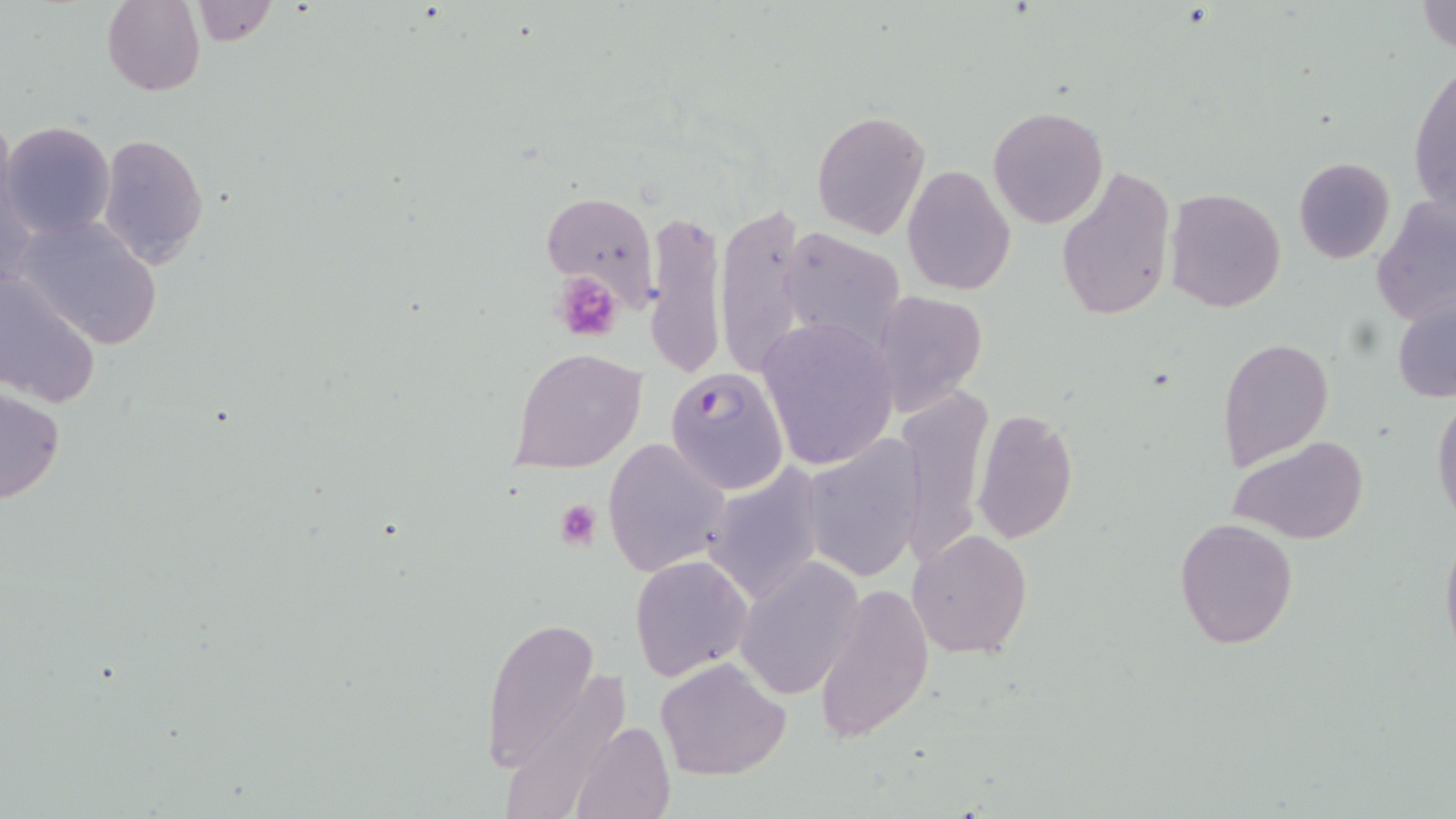

Summary:
  - Coordinate format: approximate bounding boxes as named x1/y1/x2/y2 corners in pixels
  - Platelet locations: (x1=551, y1=271, x2=627, y2=344), (x1=553, y1=500, x2=602, y2=549)
  - Uninfected red blood cell locations: (x1=1417, y1=0, x2=1456, y2=56), (x1=102, y1=1, x2=205, y2=96), (x1=187, y1=1, x2=276, y2=47), (x1=1410, y1=62, x2=1456, y2=220), (x1=988, y1=106, x2=1108, y2=227), (x1=811, y1=111, x2=931, y2=239), (x1=2, y1=120, x2=115, y2=239), (x1=98, y1=133, x2=209, y2=266), (x1=1294, y1=157, x2=1395, y2=265), (x1=901, y1=164, x2=1015, y2=297), (x1=1055, y1=164, x2=1175, y2=322), (x1=1166, y1=188, x2=1286, y2=312), (x1=541, y1=189, x2=660, y2=306), (x1=1373, y1=198, x2=1456, y2=329), (x1=716, y1=203, x2=815, y2=377), (x1=640, y1=204, x2=728, y2=381), (x1=13, y1=213, x2=164, y2=350), (x1=783, y1=232, x2=907, y2=349), (x1=0, y1=272, x2=101, y2=410), (x1=872, y1=290, x2=986, y2=414), (x1=1392, y1=292, x2=1456, y2=406), (x1=756, y1=319, x2=898, y2=471), (x1=1219, y1=336, x2=1333, y2=472), (x1=511, y1=347, x2=647, y2=474), (x1=0, y1=386, x2=65, y2=504), (x1=896, y1=386, x2=992, y2=568), (x1=1431, y1=396, x2=1456, y2=528), (x1=972, y1=409, x2=1079, y2=543), (x1=1231, y1=435, x2=1369, y2=544), (x1=799, y1=436, x2=926, y2=582), (x1=603, y1=437, x2=729, y2=578), (x1=700, y1=463, x2=830, y2=610), (x1=1174, y1=517, x2=1299, y2=651), (x1=1439, y1=526, x2=1456, y2=664), (x1=908, y1=529, x2=1033, y2=660), (x1=630, y1=552, x2=752, y2=680), (x1=737, y1=556, x2=858, y2=698), (x1=641, y1=565, x2=773, y2=766), (x1=814, y1=583, x2=936, y2=741), (x1=483, y1=616, x2=601, y2=770), (x1=656, y1=657, x2=791, y2=780), (x1=572, y1=719, x2=675, y2=819)
  - Plasmodium falciparum-infected red blood cell locations: (x1=665, y1=366, x2=790, y2=495)
  - Slide-level diagnosis: Plasmodium falciparum
  - Preparation: thin blood film
  - Modality: light microscopy
  - Magnification: 1000x
  - Stain: May-Grünwald-Giemsa
  - Image size: 1456×819 pixels
  - Field of view: single